Report the malaria status of this cell.
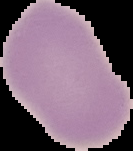

Uninfected.

image size = 133×151 pixels
image type = segmented cell region with the area outside set to black
preparation = thin blood smear